Identify the parasite.
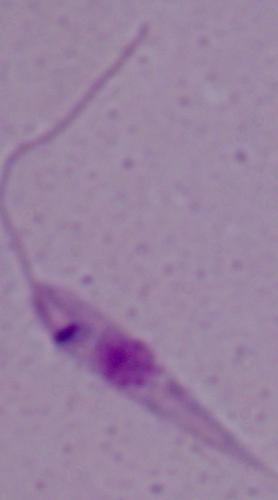
Leishmania.

Photomicrograph. 1000x magnification.